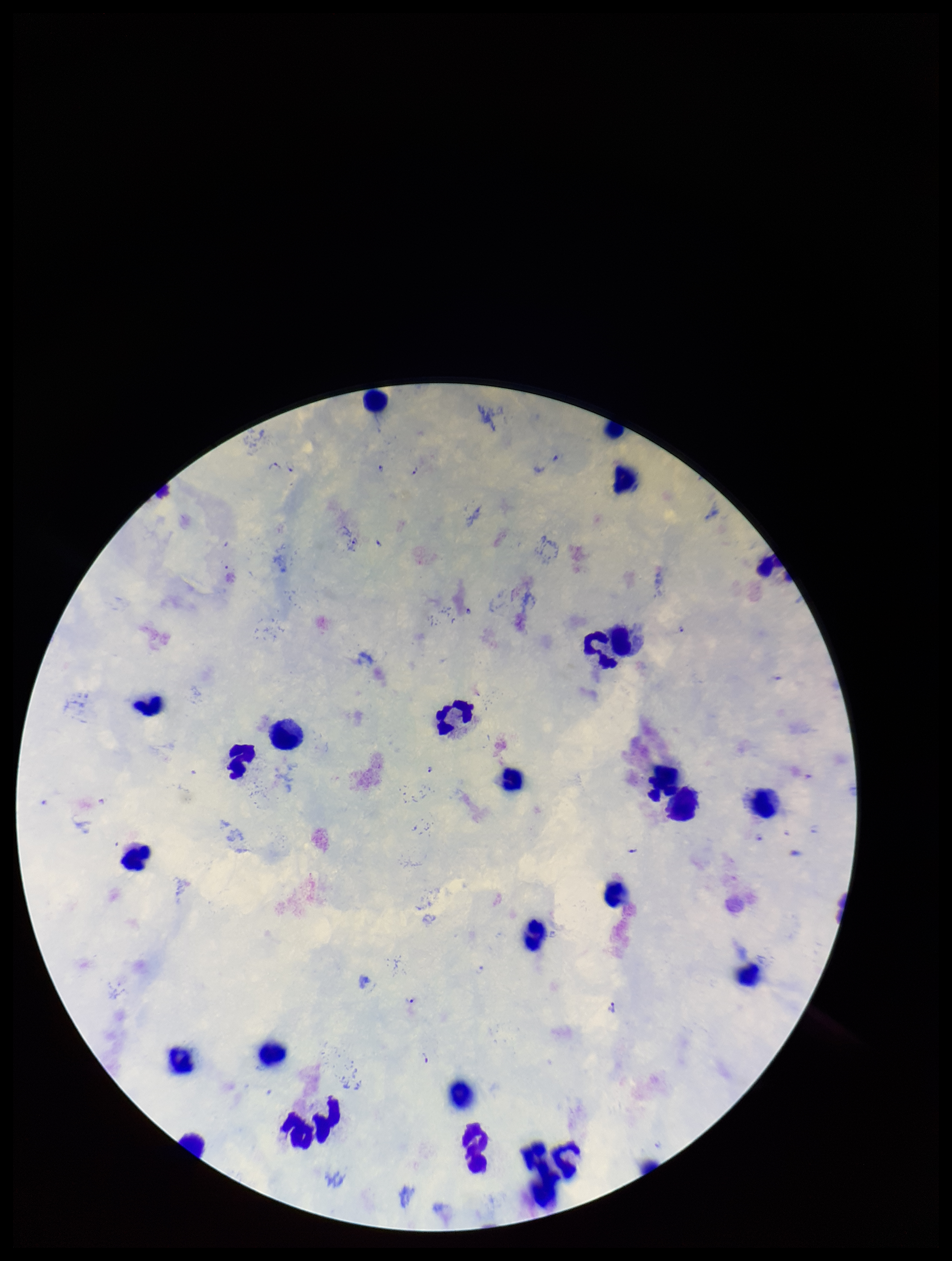 Image is 952×1261 pixels. Giemsa stain. Preparation: thick smear. Leukocyte count: 27. One field from this slide. Plasmodium parasites: seen. Species reported for this patient: Plasmodium falciparum. Smartphone photograph taken through the eyepiece of a microscope. Patient malaria status: infected. Parasite count: 16.